Evaluate for malaria.
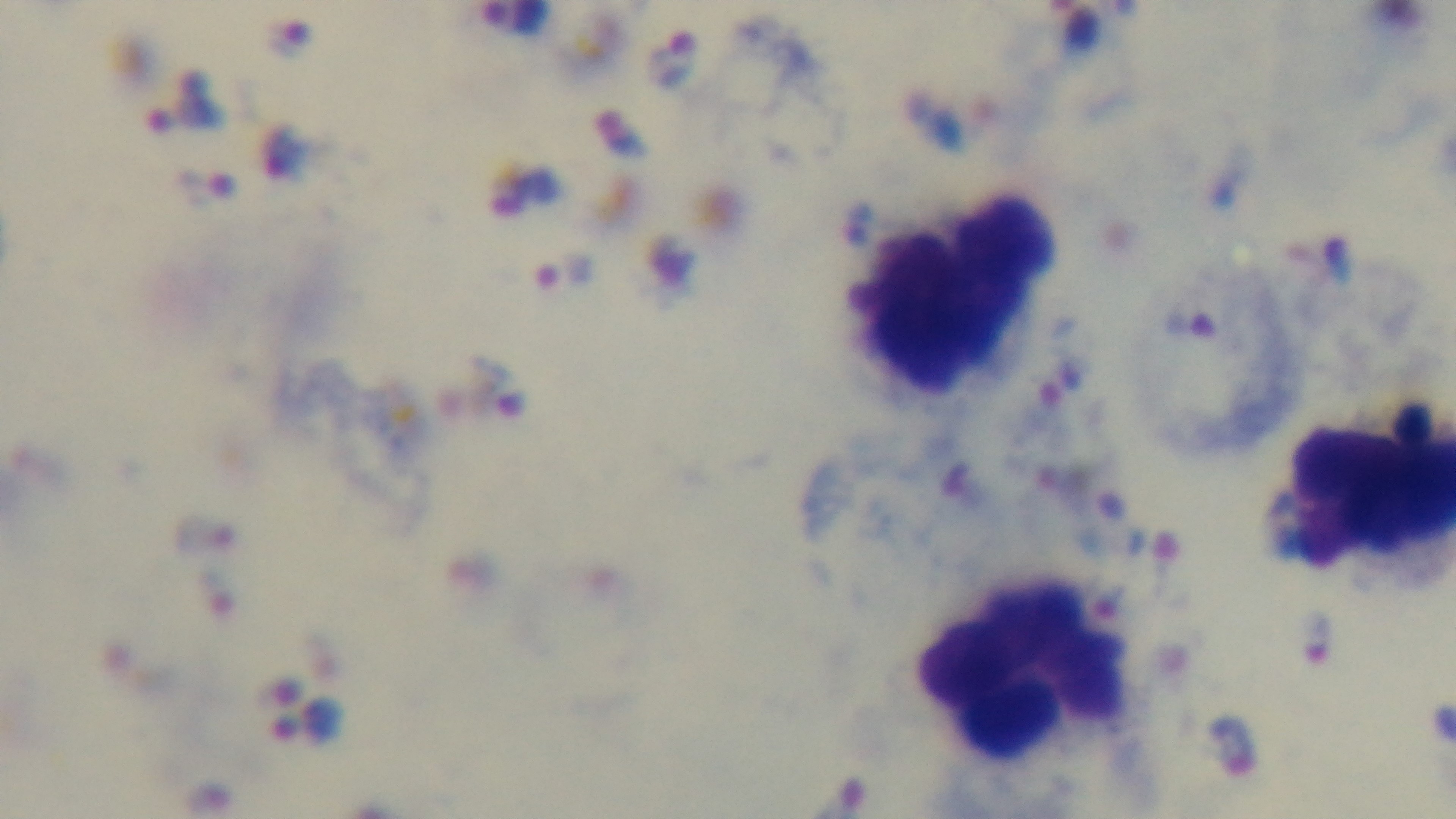

It is infected.

Single field of view. Preparation: thick smear. Oil-immersion objective, 100x. Mounted 4K digital camera. Photomicrograph. Giemsa-stained.